State which cell type is depicted.
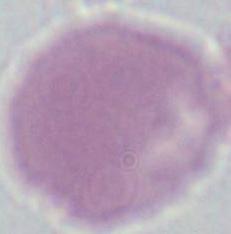

This is an erythrocyte.

Micrograph. 1000x magnification.